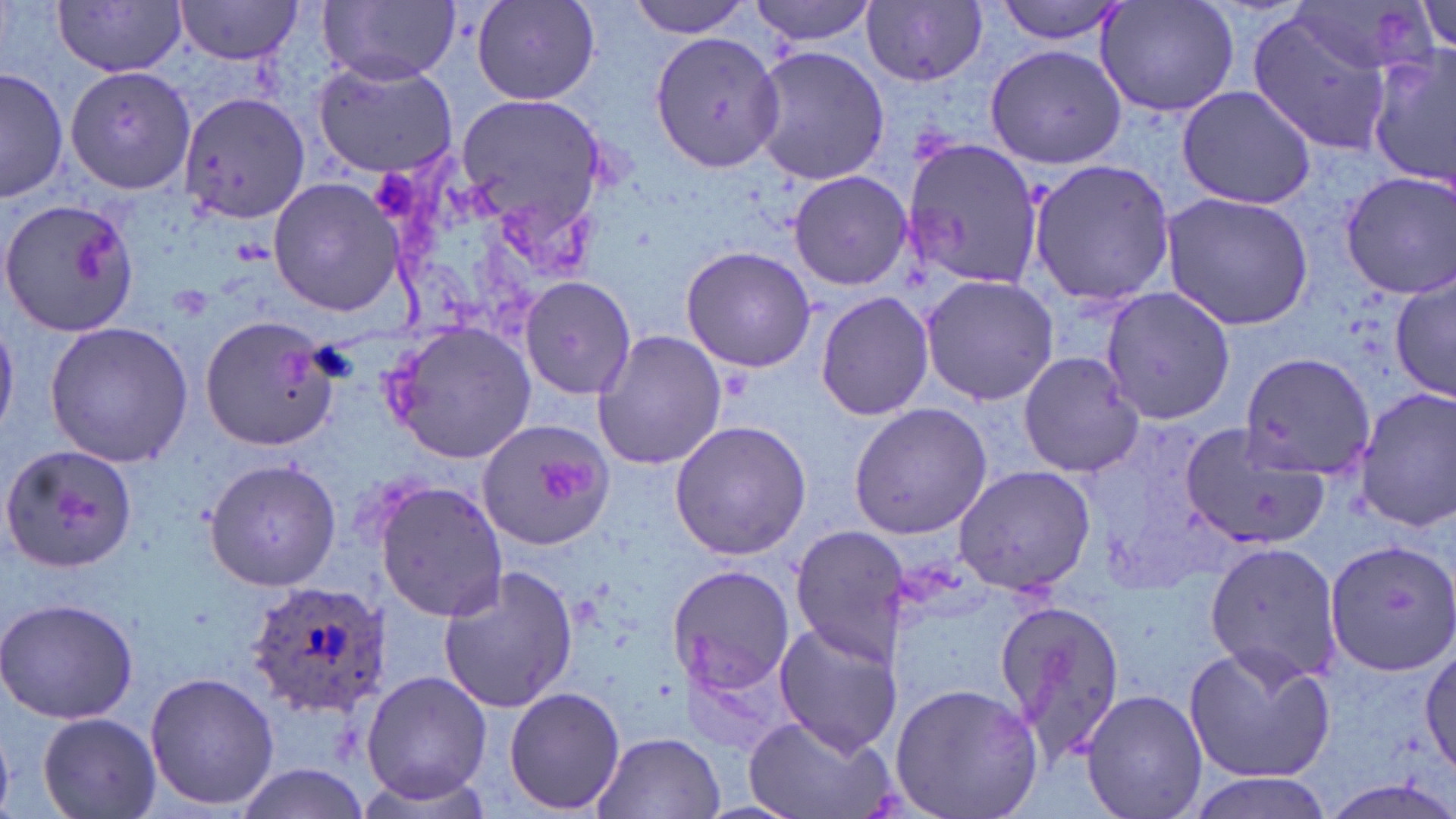

Approximate bounding boxes as (x1,y1)-(x2,y2) corner pairs in pixels. Uninfected red blood cell locations: (172,0)-(306,64), (319,0)-(461,84), (469,0)-(603,106), (624,0)-(755,37), (750,0)-(880,46), (991,0)-(1132,44), (55,1)-(188,75), (863,1)-(989,86), (1095,1)-(1241,121), (1416,2)-(1454,57), (1244,9)-(1402,156), (648,31)-(785,173), (985,43)-(1128,169), (753,47)-(888,187), (1365,51)-(1456,185), (311,58)-(459,180), (64,63)-(197,195), (2,66)-(67,202), (1175,85)-(1319,209), (180,92)-(307,225), (454,92)-(610,242), (902,135)-(1041,288), (1025,158)-(1177,308), (789,170)-(913,292), (1337,170)-(1456,299), (268,178)-(405,315), (1161,192)-(1316,329), (0,197)-(139,339), (680,246)-(816,373), (1391,270)-(1454,404), (518,274)-(637,401), (919,274)-(1060,406), (1098,285)-(1237,426), (816,290)-(935,422), (199,314)-(338,449), (382,319)-(538,462), (44,320)-(193,468), (591,330)-(730,474), (1235,350)-(1375,484), (1016,351)-(1143,477), (1354,388)-(1455,532), (848,401)-(993,540), (476,418)-(616,552), (668,420)-(810,560), (1179,421)-(1330,553), (1,444)-(138,574), (203,457)-(341,594), (954,465)-(1096,595), (376,482)-(510,622), (788,524)-(913,663), (1325,537)-(1456,676), (1203,538)-(1343,688), (436,564)-(579,714), (666,566)-(796,693), (993,596)-(1127,768), (0,597)-(139,724), (774,621)-(904,756), (1417,641)-(1456,782), (1183,642)-(1336,786), (143,671)-(279,812), (357,671)-(494,804), (889,682)-(1045,819), (502,686)-(626,814), (1080,689)-(1208,819), (37,712)-(160,819), (741,714)-(894,819), (591,732)-(725,819), (232,762)-(374,817), (1175,772)-(1338,818). Plasmodium ovale-infected red blood cell locations: (248,581)-(391,713). Slide-level diagnosis: Plasmodium ovale. Light microscopy. Single field of view. Image is 1456×819 pixels. 1000x magnification. Thin blood film. May-Grünwald-Giemsa stain.